Point out each Plasmodium parasite.
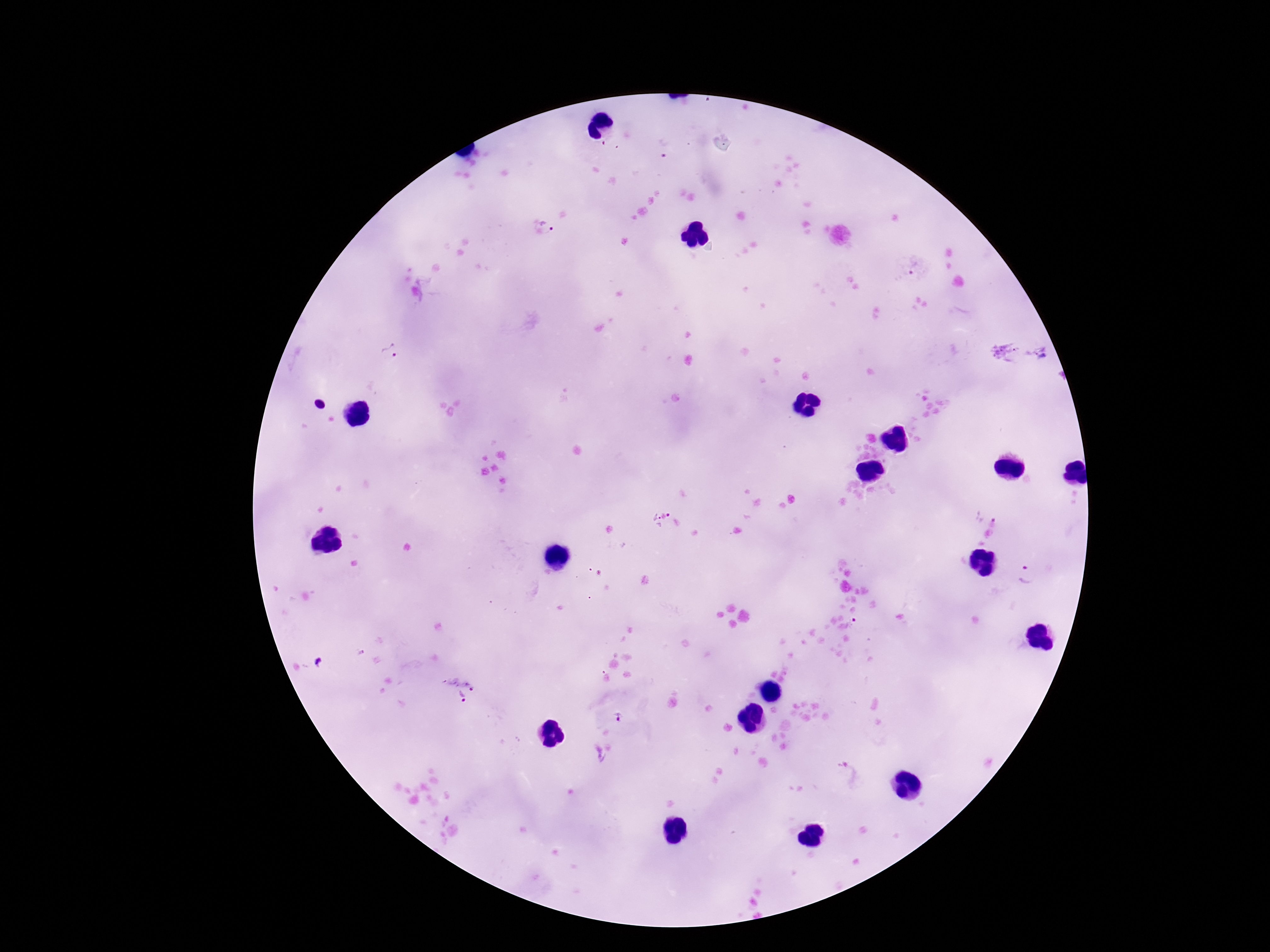

Approximate object centers, in pixels from the top-left corner.
Plasmodium parasites: (x=546, y=227), (x=914, y=269), (x=391, y=351), (x=987, y=511), (x=670, y=514), (x=653, y=523), (x=1024, y=574), (x=855, y=622), (x=470, y=682), (x=461, y=695), (x=618, y=717), (x=847, y=774).

Summary:
  - Field of view: one from this slide
  - Image size: 1270×952 pixels
  - Capture: smartphone camera through the microscope eyepiece
  - Magnification: 100x
  - Preparation: thick peripheral-blood smear
  - Patient malaria status: infected
  - Stain: Giemsa